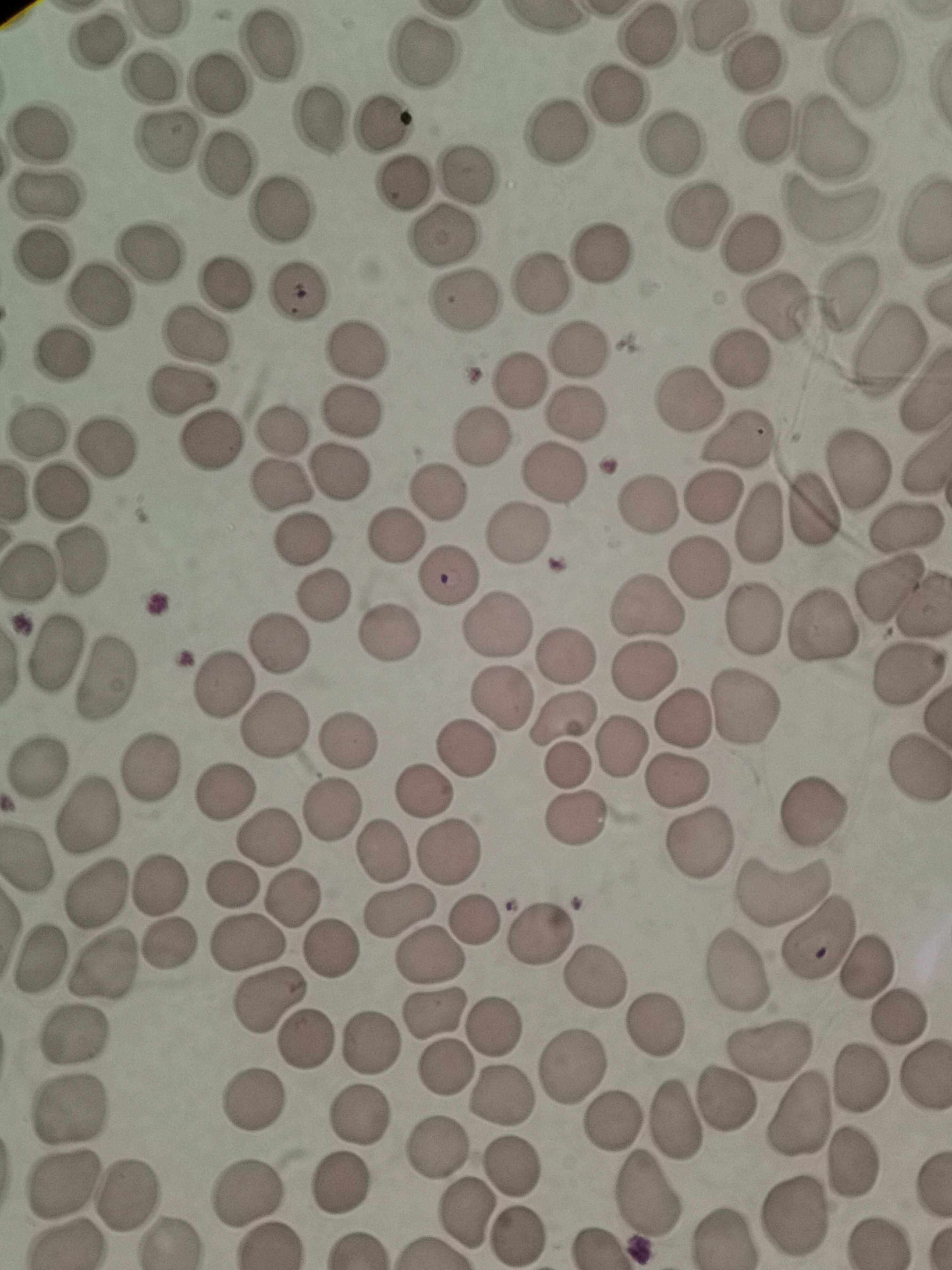

Approximate centers as [x, y] in pixels. Cell locations: [647, 36], [95, 41], [268, 45], [422, 56], [860, 60], [753, 63], [149, 78], [222, 82], [616, 94], [317, 120], [380, 120], [555, 129], [766, 132], [42, 134], [835, 136], [164, 140], [673, 142], [225, 163], [472, 173], [403, 179], [47, 195], [281, 210], [832, 211], [694, 215], [442, 235], [750, 247], [598, 250], [147, 251], [44, 256], [224, 282], [539, 284], [294, 290], [848, 291], [99, 295], [461, 303], [776, 308], [198, 334], [356, 349], [578, 349], [889, 349], [61, 353], [739, 354], [520, 379], [184, 393], [689, 398], [579, 410], [350, 415], [280, 429], [39, 431], [480, 437], [211, 438], [739, 440], [103, 446], [552, 472], [856, 472], [342, 473], [283, 482], [64, 490], [438, 493], [712, 498], [646, 503], [813, 509], [758, 520], [905, 527], [517, 535], [393, 537], [304, 540], [78, 560], [701, 567], [447, 576], [891, 586], [319, 595], [651, 608], [750, 617], [494, 622], [821, 625], [390, 638], [279, 642], [54, 651], [566, 655], [643, 670], [908, 674], [107, 680], [222, 684], [503, 699], [746, 708], [563, 717], [682, 717], [276, 724], [349, 736], [622, 743], [464, 744], [566, 767], [42, 768], [146, 769], [917, 774], [677, 778], [226, 793], [422, 796], [335, 809], [813, 810], [86, 818], [579, 820], [270, 837], [699, 840], [447, 851], [382, 853], [161, 884], [229, 885], [781, 891], [95, 894], [291, 899], [397, 912], [474, 919], [542, 930], [819, 938], [248, 944], [168, 948], [330, 948], [430, 957], [38, 962], [103, 965], [737, 968], [868, 970], [597, 976], [267, 1000], [434, 1014], [899, 1020], [656, 1021], [496, 1025], [76, 1036], [307, 1039], [370, 1045], [768, 1052], [574, 1064], [445, 1069], [920, 1075], [858, 1082], [504, 1094], [252, 1100], [727, 1101], [70, 1112], [796, 1113], [357, 1116], [614, 1118], [676, 1119], [436, 1150], [852, 1163], [511, 1166], [342, 1186], [64, 1187], [250, 1191], [647, 1195], [130, 1197], [468, 1210], [795, 1213], [516, 1236], [725, 1237]. Single field of view. Acquired by smartphone through the microscope eyepiece. Thin blood film. Giemsa-stained preparation. Image is 952×1270 pixels.